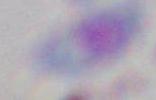
Summary:
  - Identification: Toxoplasma gondii
  - Magnification: 1000x
  - Modality: micrograph